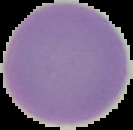 Image is 133×130 pixels. Result: no malaria parasites detected. Cell region segmented out of the field of view; the surrounding area is masked to black. From a thin blood smear.